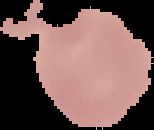

preparation: thin blood film
image_type: segmented cell region on a black background
image_size: 154×130 pixels
result: negative for malaria parasites